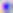
Summary:
  - Identification: Toxoplasma gondii
  - Modality: photomicrograph
  - Magnification: 400x